State the blood parasite species.
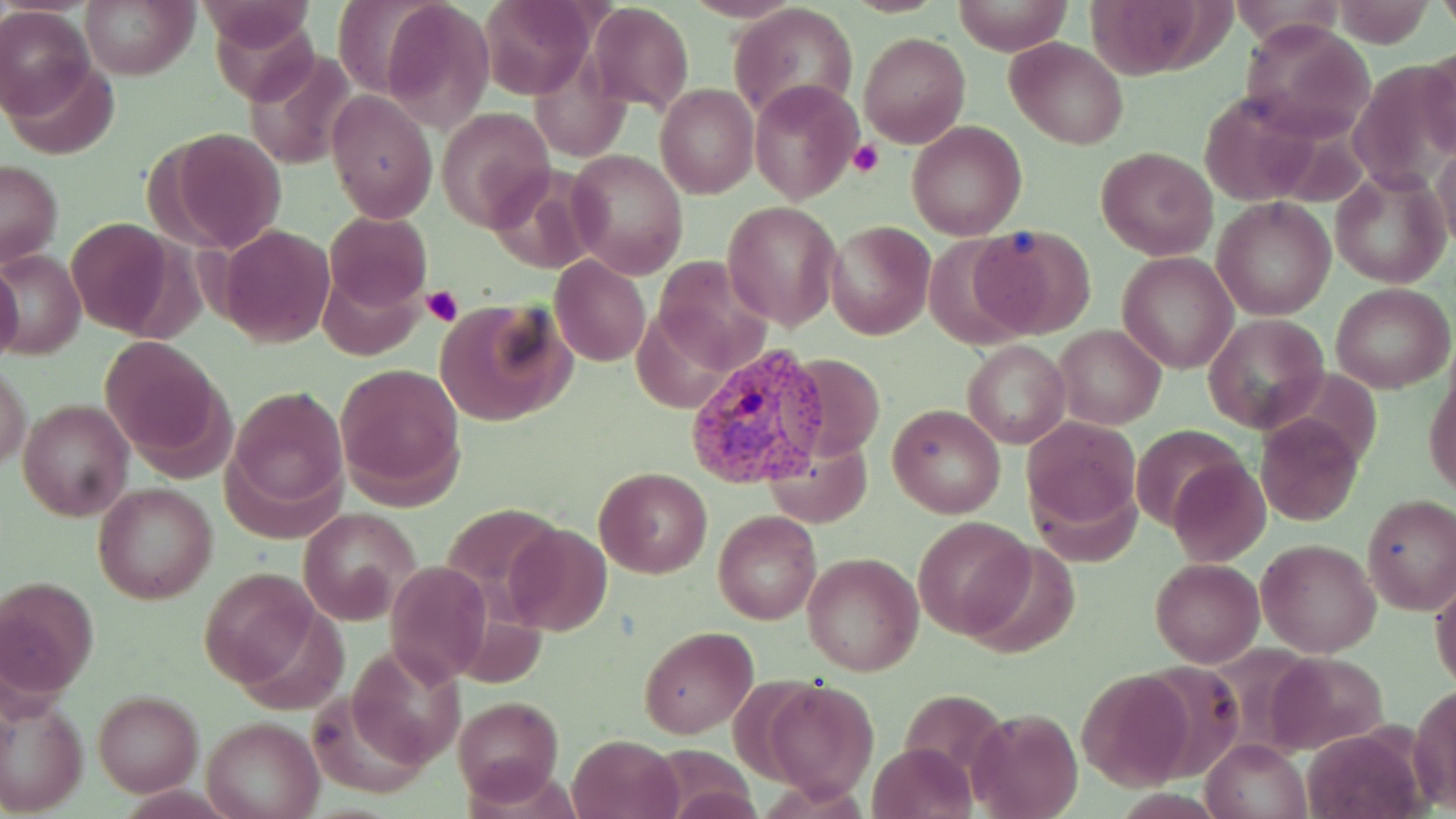

Plasmodium vivax.

Approximate bounding boxes as (x1, y1, x2, y2) in pixels. Uninfected red blood cell locations: (78, 0, 198, 81), (381, 0, 496, 133), (952, 0, 1073, 56), (333, 1, 444, 100), (480, 1, 590, 98), (586, 2, 693, 111), (731, 2, 859, 121), (0, 5, 94, 120), (1236, 20, 1376, 142), (859, 31, 970, 148), (1005, 38, 1127, 150), (1419, 45, 1456, 162), (244, 47, 356, 168), (3, 59, 121, 161), (749, 78, 863, 204), (655, 84, 758, 198), (327, 92, 436, 221), (437, 107, 552, 230), (907, 122, 1028, 241), (165, 130, 287, 253), (1434, 142, 1456, 252), (1096, 147, 1216, 259), (567, 149, 687, 278), (1, 159, 63, 265), (1330, 164, 1452, 290), (486, 165, 602, 274), (1211, 197, 1336, 321), (723, 201, 841, 330), (325, 212, 433, 311), (65, 216, 177, 334), (826, 222, 933, 339), (219, 225, 334, 348), (975, 226, 1092, 338), (2, 252, 86, 358), (1116, 252, 1237, 375), (550, 256, 650, 366), (0, 262, 23, 365), (1331, 284, 1453, 393), (434, 300, 573, 427), (1203, 313, 1330, 435), (1055, 325, 1165, 430), (102, 336, 224, 456), (964, 339, 1070, 449), (782, 353, 887, 463), (336, 362, 467, 504), (1426, 363, 1455, 499), (1, 364, 31, 471), (227, 385, 348, 514), (18, 397, 134, 523), (887, 403, 1006, 518), (1255, 413, 1362, 526), (1020, 415, 1141, 540), (1134, 424, 1242, 531), (763, 436, 873, 528), (1171, 458, 1270, 565), (594, 467, 711, 578), (92, 482, 217, 603), (1362, 495, 1456, 615), (297, 509, 417, 620), (714, 511, 822, 625), (912, 516, 1033, 639), (504, 524, 612, 635), (1257, 537, 1381, 657), (965, 540, 1078, 658), (803, 552, 923, 676), (1150, 558, 1263, 667), (388, 561, 490, 685), (197, 566, 321, 688), (0, 575, 100, 701), (1431, 579, 1456, 695), (639, 626, 758, 739), (1076, 671, 1195, 789), (2, 678, 89, 819), (760, 680, 879, 802), (1410, 684, 1456, 812), (93, 689, 203, 797), (452, 696, 563, 805), (969, 708, 1082, 819), (202, 716, 323, 819), (1299, 727, 1431, 819), (569, 734, 681, 819), (1203, 736, 1311, 819), (868, 743, 976, 818). Plasmodium vivax-infected red blood cell locations: (685, 342, 827, 488). Platelet locations: (851, 141, 883, 178), (421, 286, 463, 328). Image is 1456×819 pixels. Single field of view. 1000x magnification. May-Grünwald-Giemsa stain. Thin blood smear. Optical microscopy.